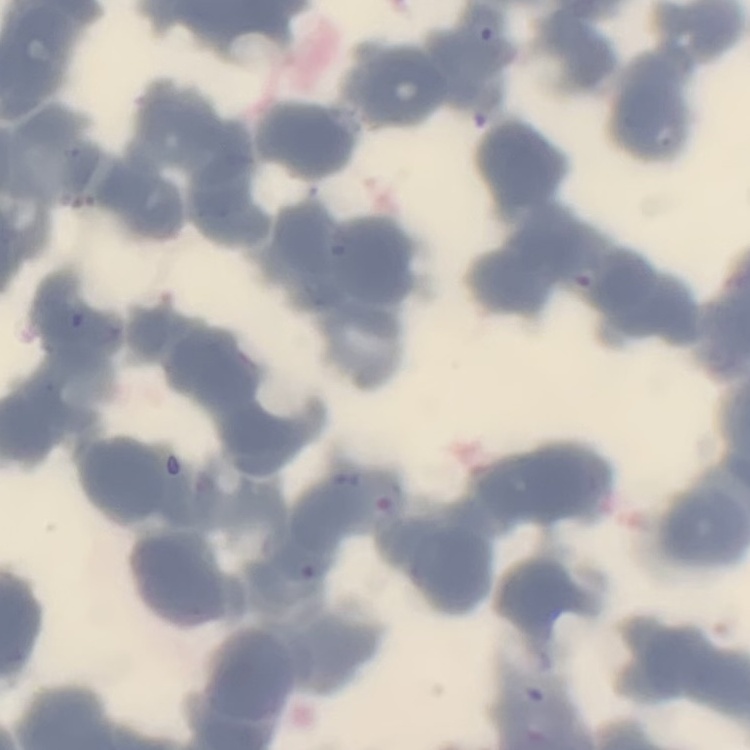
red blood cell morphology = rouleaux formation
preparation = thin peripheral smear
stain = Field's or Giemsa
image type = one tile cut from a larger photomicrograph